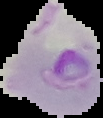 From a thin blood smear. Cell region segmented out of the field of view; the surrounding area is masked to black. Malaria status: parasitized. Image is 103×118 pixels.